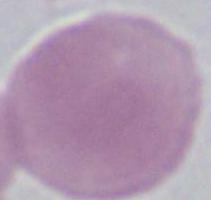
1000x magnification. Photomicrograph. An erythrocyte is shown.